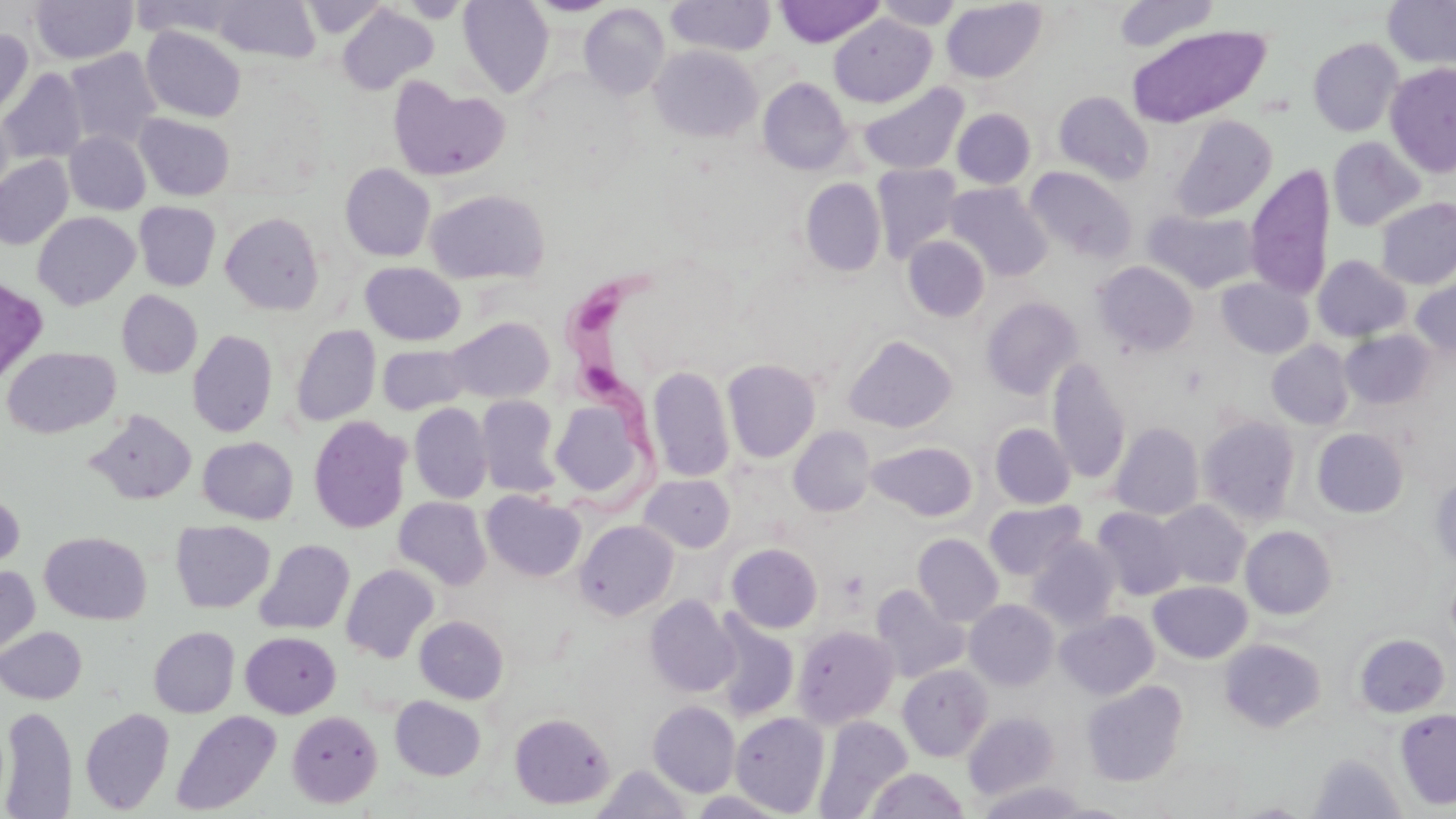

Approximate bounding boxes as (x1, y1, x2, y2) in pixels. Trypanosoma brucei locations: (544, 261, 682, 526). Uninfected red blood cell locations: (30, 0, 137, 65), (130, 0, 245, 39), (211, 0, 321, 64), (300, 0, 391, 39), (399, 0, 470, 23), (458, 0, 553, 97), (529, 0, 618, 17), (666, 0, 776, 56), (775, 0, 885, 47), (1113, 0, 1219, 53), (1383, 0, 1456, 70), (874, 1, 963, 30), (941, 1, 1046, 83), (579, 4, 670, 99), (336, 5, 438, 95), (829, 14, 936, 107), (1126, 25, 1271, 128), (141, 26, 246, 122), (0, 28, 33, 122), (1308, 37, 1404, 137), (650, 45, 762, 142), (65, 48, 162, 149), (1385, 62, 1456, 177), (0, 69, 87, 164), (758, 77, 852, 174), (389, 78, 511, 181), (859, 83, 968, 175), (1054, 91, 1154, 185), (0, 107, 15, 200), (952, 109, 1035, 189), (135, 114, 235, 200), (1172, 116, 1277, 220), (64, 131, 151, 215), (1327, 137, 1425, 231), (0, 156, 73, 249), (340, 163, 435, 261), (872, 164, 963, 262), (1245, 164, 1335, 302), (1027, 167, 1137, 263), (800, 178, 886, 277), (946, 182, 1052, 281), (425, 189, 550, 285), (1376, 198, 1456, 289), (134, 202, 221, 291), (1144, 209, 1260, 293), (32, 212, 140, 310), (220, 212, 324, 314), (903, 236, 990, 322), (1313, 255, 1411, 342), (1092, 261, 1198, 357), (360, 262, 466, 345), (0, 274, 49, 390), (1411, 276, 1456, 360), (1217, 278, 1313, 358), (117, 290, 203, 378), (981, 296, 1083, 399), (444, 317, 555, 404), (291, 324, 380, 426), (187, 329, 278, 437), (1340, 330, 1437, 410), (843, 335, 957, 433), (1267, 340, 1354, 430), (377, 343, 472, 414), (2, 346, 120, 438), (1047, 357, 1131, 485), (722, 358, 821, 463), (648, 365, 734, 483), (476, 394, 562, 498), (550, 400, 647, 499), (409, 403, 492, 504), (87, 410, 197, 505), (308, 415, 412, 534), (1198, 416, 1301, 525), (1110, 422, 1204, 520), (990, 423, 1076, 509), (788, 426, 876, 517), (1312, 428, 1408, 518), (198, 436, 298, 524), (867, 441, 978, 521), (639, 473, 735, 553), (1430, 474, 1456, 569), (0, 488, 25, 574), (482, 491, 586, 582), (393, 497, 491, 590), (1152, 500, 1250, 589), (983, 501, 1086, 580), (1093, 507, 1186, 600), (574, 519, 678, 620), (171, 520, 275, 613), (1241, 525, 1337, 619), (39, 531, 151, 624), (912, 533, 1003, 626), (1028, 536, 1122, 630), (254, 539, 354, 635), (726, 543, 823, 632), (341, 564, 439, 663), (0, 565, 41, 658), (1148, 581, 1252, 663), (870, 584, 970, 683), (645, 596, 740, 697), (965, 600, 1059, 689), (1056, 610, 1159, 699), (709, 612, 800, 722), (415, 616, 509, 703), (793, 625, 899, 727), (0, 626, 87, 704), (149, 627, 239, 717), (241, 632, 340, 718), (1353, 633, 1450, 718), (1220, 638, 1325, 732), (897, 664, 993, 761), (1082, 681, 1187, 786), (390, 696, 485, 780), (648, 701, 740, 797), (1, 705, 79, 819), (80, 708, 175, 814), (1395, 709, 1456, 810), (171, 710, 281, 815), (287, 710, 382, 807), (963, 711, 1060, 800), (509, 712, 614, 809), (731, 712, 830, 816), (814, 715, 913, 817), (1308, 752, 1406, 819), (593, 764, 693, 819), (867, 767, 969, 819), (976, 780, 1088, 819). Platelet locations: (838, 570, 869, 599). Slide-level diagnosis: Trypanosoma brucei. Optical microscopy. May-Grünwald-Giemsa stain. Image is 1456×819 pixels. Thin blood smear. 1000x magnification. Single field of view.